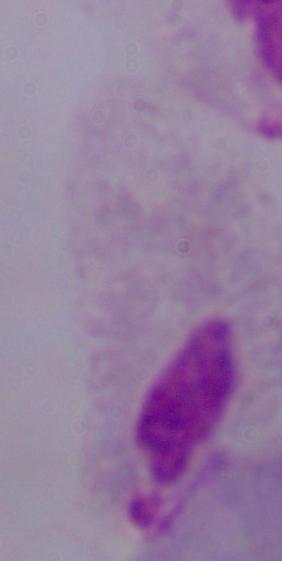
magnification: 1000x
modality: photomicrograph
identification: trichomonad